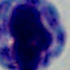

Summary:
  - Identification: white blood cell
  - Modality: photomicrograph
  - Magnification: 1000x